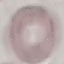 Result: no malaria parasites detected. Cell patch, automatically extracted from a larger field of view and resized to 64 × 64 pixels. Photographed with a smartphone camera at the microscope eyepiece. Giemsa-stained preparation. Thin smear of blood.